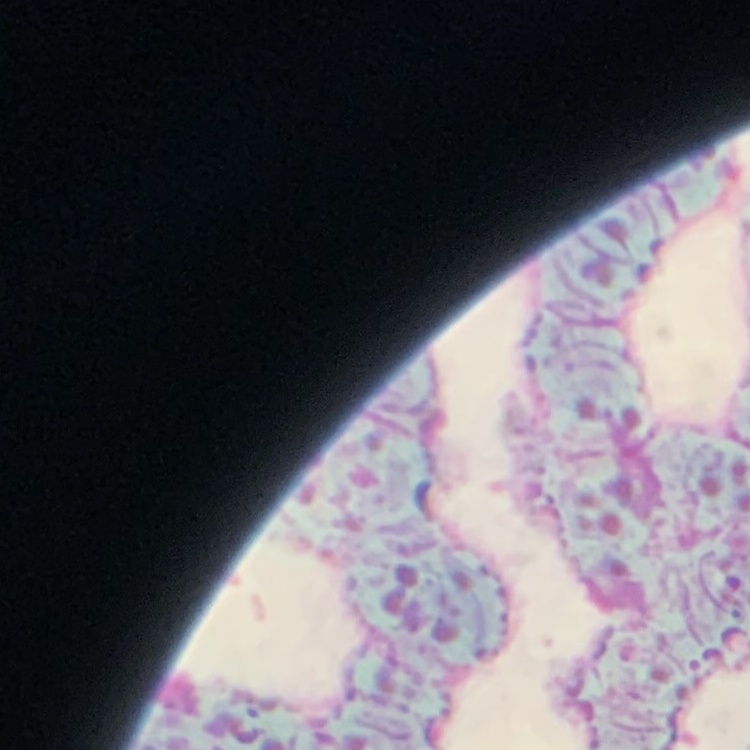

The erythrocytes exhibit rouleaux formation. Square crop of a larger photomicrograph. Thin peripheral smear. Stained with either Field's or Giemsa.